Classify this cell by malaria status.
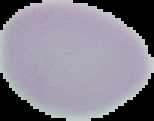

Uninfected.

{
  "preparation": "thin blood smear",
  "image_size": "154×121 pixels",
  "image_type": "cell region segmented out of the field of view; surrounding area masked to black"
}